Locate every uninfected red blood cell.
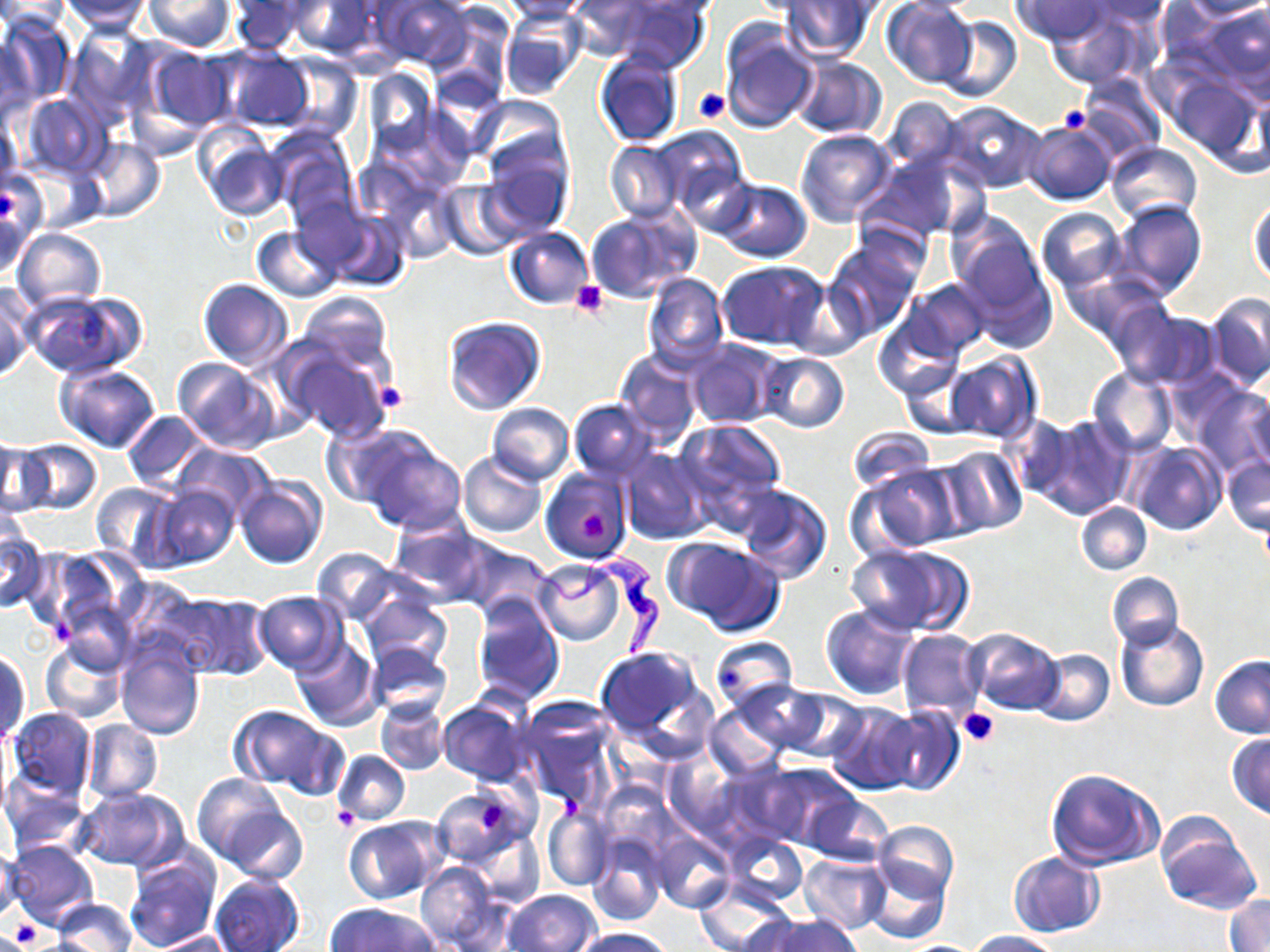
Approximate bounding boxes as named x1/y1/x2/y2 corners in pixels.
Uninfected red blood cells: (x1=0, y1=0, x2=70, y2=32), (x1=374, y1=0, x2=472, y2=68), (x1=499, y1=0, x2=596, y2=22), (x1=566, y1=0, x2=658, y2=60), (x1=605, y1=0, x2=708, y2=72), (x1=881, y1=0, x2=977, y2=87), (x1=1011, y1=0, x2=1114, y2=45), (x1=1078, y1=0, x2=1174, y2=28), (x1=57, y1=1, x2=153, y2=32), (x1=144, y1=1, x2=235, y2=52), (x1=285, y1=1, x2=376, y2=57), (x1=779, y1=1, x2=878, y2=60), (x1=1182, y1=1, x2=1270, y2=21), (x1=228, y1=2, x2=309, y2=54), (x1=1194, y1=3, x2=1269, y2=89), (x1=1044, y1=5, x2=1152, y2=87), (x1=501, y1=11, x2=588, y2=100), (x1=2, y1=14, x2=75, y2=109), (x1=938, y1=16, x2=1022, y2=102), (x1=66, y1=25, x2=153, y2=124), (x1=719, y1=25, x2=818, y2=134), (x1=0, y1=33, x2=37, y2=124), (x1=142, y1=46, x2=235, y2=135), (x1=216, y1=47, x2=314, y2=132), (x1=594, y1=51, x2=684, y2=149), (x1=275, y1=53, x2=362, y2=142), (x1=790, y1=55, x2=887, y2=137), (x1=364, y1=68, x2=436, y2=155), (x1=1077, y1=73, x2=1166, y2=161), (x1=1165, y1=77, x2=1262, y2=173), (x1=19, y1=93, x2=112, y2=178), (x1=880, y1=95, x2=966, y2=174), (x1=471, y1=97, x2=570, y2=183), (x1=943, y1=102, x2=1046, y2=191), (x1=0, y1=112, x2=22, y2=191), (x1=1025, y1=120, x2=1117, y2=205), (x1=649, y1=125, x2=748, y2=217), (x1=796, y1=129, x2=896, y2=228), (x1=269, y1=131, x2=358, y2=227), (x1=197, y1=132, x2=287, y2=220), (x1=82, y1=137, x2=165, y2=222), (x1=605, y1=141, x2=685, y2=223), (x1=1108, y1=141, x2=1201, y2=224), (x1=479, y1=151, x2=574, y2=237), (x1=860, y1=154, x2=971, y2=243), (x1=1, y1=174, x2=38, y2=277), (x1=714, y1=178, x2=812, y2=262), (x1=441, y1=181, x2=524, y2=259), (x1=383, y1=185, x2=461, y2=263), (x1=291, y1=195, x2=373, y2=278), (x1=1110, y1=199, x2=1207, y2=301), (x1=1248, y1=199, x2=1270, y2=287), (x1=585, y1=207, x2=698, y2=303), (x1=1037, y1=207, x2=1128, y2=292), (x1=322, y1=209, x2=411, y2=291), (x1=952, y1=223, x2=1053, y2=342), (x1=252, y1=226, x2=341, y2=302), (x1=506, y1=226, x2=594, y2=308), (x1=13, y1=227, x2=106, y2=311), (x1=824, y1=237, x2=923, y2=339), (x1=718, y1=261, x2=830, y2=350), (x1=643, y1=272, x2=728, y2=370), (x1=197, y1=278, x2=293, y2=369), (x1=787, y1=279, x2=870, y2=360), (x1=904, y1=279, x2=993, y2=360), (x1=0, y1=284, x2=34, y2=382), (x1=23, y1=289, x2=145, y2=379), (x1=296, y1=290, x2=394, y2=382), (x1=1205, y1=292, x2=1270, y2=390), (x1=1109, y1=303, x2=1217, y2=389), (x1=872, y1=315, x2=964, y2=402), (x1=443, y1=316, x2=545, y2=414), (x1=686, y1=338, x2=781, y2=429), (x1=282, y1=341, x2=396, y2=444), (x1=615, y1=350, x2=703, y2=447), (x1=757, y1=352, x2=850, y2=432), (x1=945, y1=353, x2=1040, y2=443), (x1=173, y1=358, x2=280, y2=455), (x1=54, y1=363, x2=160, y2=454), (x1=900, y1=365, x2=980, y2=437), (x1=1088, y1=368, x2=1177, y2=457), (x1=1194, y1=385, x2=1270, y2=474), (x1=1244, y1=395, x2=1270, y2=474), (x1=568, y1=399, x2=657, y2=480), (x1=486, y1=402, x2=575, y2=485), (x1=122, y1=410, x2=212, y2=490), (x1=1000, y1=414, x2=1080, y2=500), (x1=1031, y1=416, x2=1134, y2=519), (x1=673, y1=420, x2=786, y2=519), (x1=322, y1=422, x2=424, y2=511), (x1=352, y1=427, x2=467, y2=533), (x1=848, y1=427, x2=933, y2=493), (x1=1, y1=439, x2=45, y2=519), (x1=18, y1=439, x2=102, y2=516), (x1=1130, y1=441, x2=1226, y2=535), (x1=175, y1=443, x2=275, y2=522), (x1=935, y1=446, x2=1029, y2=536), (x1=620, y1=448, x2=712, y2=545), (x1=459, y1=452, x2=547, y2=539), (x1=1223, y1=453, x2=1269, y2=536), (x1=853, y1=463, x2=964, y2=555), (x1=542, y1=468, x2=632, y2=564), (x1=235, y1=476, x2=326, y2=570), (x1=89, y1=481, x2=177, y2=568), (x1=734, y1=484, x2=833, y2=584), (x1=148, y1=485, x2=240, y2=569), (x1=1076, y1=501, x2=1152, y2=575), (x1=387, y1=516, x2=492, y2=606), (x1=0, y1=523, x2=46, y2=613), (x1=665, y1=537, x2=785, y2=637), (x1=460, y1=542, x2=554, y2=619), (x1=848, y1=543, x2=971, y2=636), (x1=311, y1=547, x2=400, y2=625), (x1=27, y1=548, x2=130, y2=639), (x1=533, y1=560, x2=629, y2=644), (x1=1107, y1=572, x2=1184, y2=650), (x1=253, y1=591, x2=346, y2=674), (x1=163, y1=592, x2=271, y2=680), (x1=358, y1=592, x2=451, y2=674), (x1=472, y1=596, x2=563, y2=703), (x1=820, y1=605, x2=921, y2=700), (x1=1115, y1=618, x2=1208, y2=712), (x1=896, y1=628, x2=985, y2=721), (x1=963, y1=628, x2=1063, y2=714), (x1=39, y1=635, x2=127, y2=725), (x1=709, y1=636, x2=798, y2=712), (x1=289, y1=637, x2=380, y2=731), (x1=116, y1=641, x2=206, y2=741), (x1=364, y1=643, x2=453, y2=720), (x1=594, y1=646, x2=715, y2=760), (x1=1031, y1=649, x2=1114, y2=725), (x1=1, y1=650, x2=30, y2=747), (x1=1210, y1=655, x2=1270, y2=738), (x1=729, y1=679, x2=829, y2=755), (x1=784, y1=693, x2=869, y2=763), (x1=437, y1=697, x2=534, y2=787), (x1=376, y1=699, x2=450, y2=775), (x1=512, y1=700, x2=620, y2=808), (x1=826, y1=702, x2=922, y2=794), (x1=228, y1=704, x2=338, y2=793), (x1=706, y1=704, x2=787, y2=781), (x1=880, y1=706, x2=964, y2=797), (x1=7, y1=707, x2=96, y2=800), (x1=81, y1=720, x2=163, y2=803), (x1=1229, y1=734, x2=1270, y2=818), (x1=333, y1=750, x2=409, y2=826), (x1=663, y1=755, x2=741, y2=838), (x1=730, y1=759, x2=854, y2=849), (x1=1044, y1=768, x2=1165, y2=872), (x1=193, y1=773, x2=290, y2=866), (x1=2, y1=774, x2=90, y2=858), (x1=433, y1=786, x2=525, y2=866), (x1=76, y1=787, x2=188, y2=872), (x1=804, y1=794, x2=892, y2=865), (x1=222, y1=805, x2=308, y2=884), (x1=543, y1=808, x2=613, y2=890), (x1=1154, y1=815, x2=1263, y2=915), (x1=344, y1=816, x2=447, y2=904), (x1=872, y1=821, x2=958, y2=906), (x1=472, y1=829, x2=545, y2=909), (x1=652, y1=831, x2=734, y2=913), (x1=586, y1=832, x2=668, y2=925), (x1=721, y1=833, x2=808, y2=908), (x1=6, y1=840, x2=99, y2=930), (x1=0, y1=844, x2=21, y2=924), (x1=1008, y1=851, x2=1105, y2=938), (x1=799, y1=853, x2=891, y2=934), (x1=123, y1=854, x2=218, y2=952), (x1=864, y1=857, x2=950, y2=944), (x1=417, y1=861, x2=501, y2=951), (x1=210, y1=874, x2=305, y2=952), (x1=694, y1=882, x2=795, y2=952), (x1=505, y1=889, x2=600, y2=952), (x1=1226, y1=894, x2=1270, y2=952), (x1=50, y1=899, x2=137, y2=952), (x1=327, y1=904, x2=439, y2=952), (x1=765, y1=914, x2=858, y2=952), (x1=575, y1=927, x2=675, y2=951), (x1=149, y1=930, x2=235, y2=951), (x1=963, y1=930, x2=1062, y2=951).

Platelet locations: (x1=694, y1=89, x2=730, y2=124), (x1=1059, y1=104, x2=1090, y2=132), (x1=571, y1=280, x2=607, y2=319), (x1=375, y1=383, x2=407, y2=415), (x1=959, y1=707, x2=1000, y2=743), (x1=559, y1=794, x2=586, y2=821), (x1=479, y1=803, x2=508, y2=833), (x1=330, y1=808, x2=359, y2=832), (x1=8, y1=925, x2=41, y2=949). Trypanosoma brucei locations: (x1=523, y1=549, x2=663, y2=659). Slide-level diagnosis: Trypanosoma brucei. One field of a larger specimen. 1000x magnification. Image is 1270×952 pixels. Thin blood film. Light microscopy. May-Grünwald-Giemsa stain.